Assess the morphology of the erythrocytes.
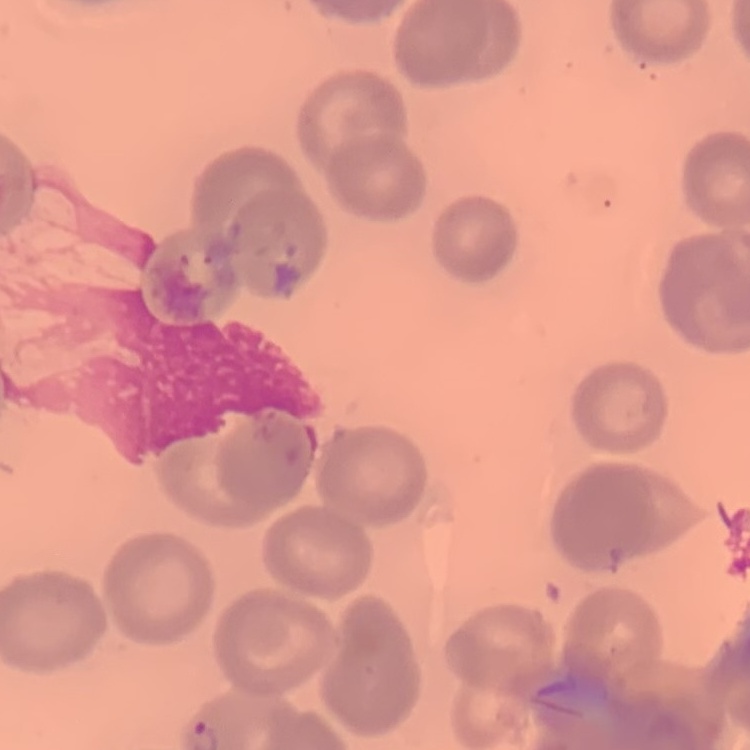
They show no rouleaux formation.

One tile cut from a larger photomicrograph. Thin blood smear. Field's or Giemsa stain.